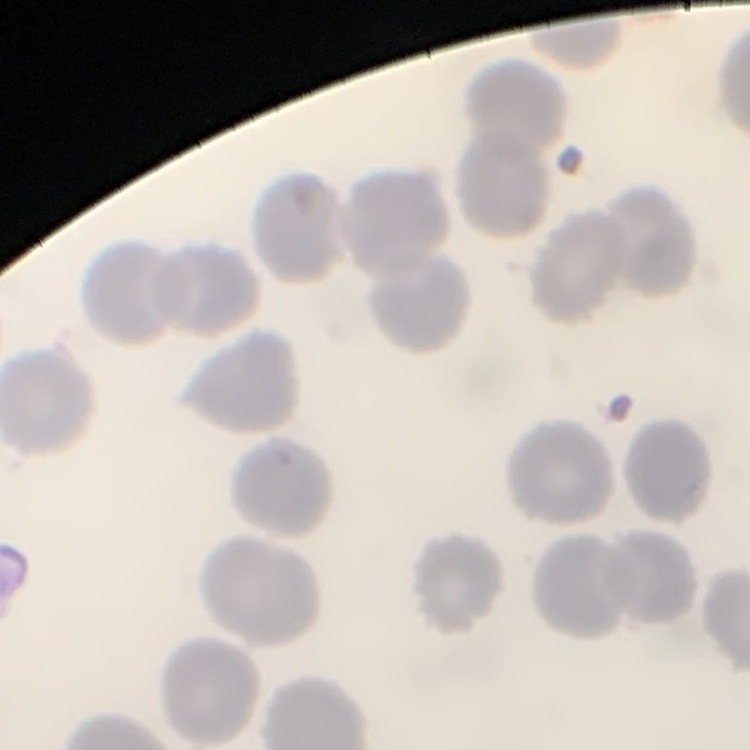

erythrocyte_morphology: no rouleaux formation
preparation: thin blood smear
image_type: one tile cut from a larger photomicrograph
stain: Field's or Giemsa